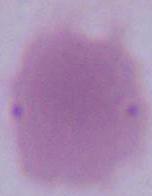

1000x magnification. Photomicrograph. An erythrocyte is shown.